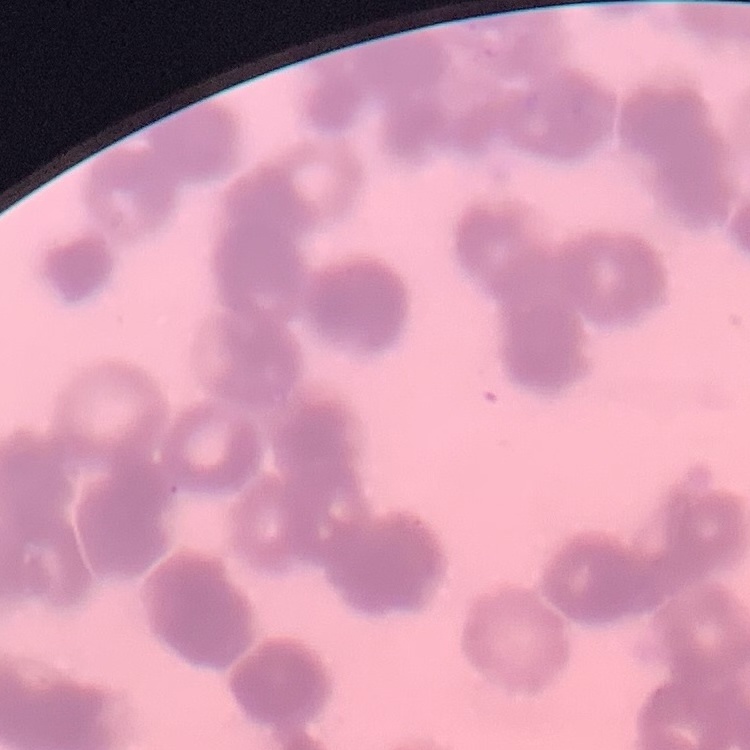
erythrocyte morphology = rouleaux formation
image type = one tile cut from a larger photomicrograph
preparation = thin blood smear
stain = Field's or Giemsa